Rate the background quality.
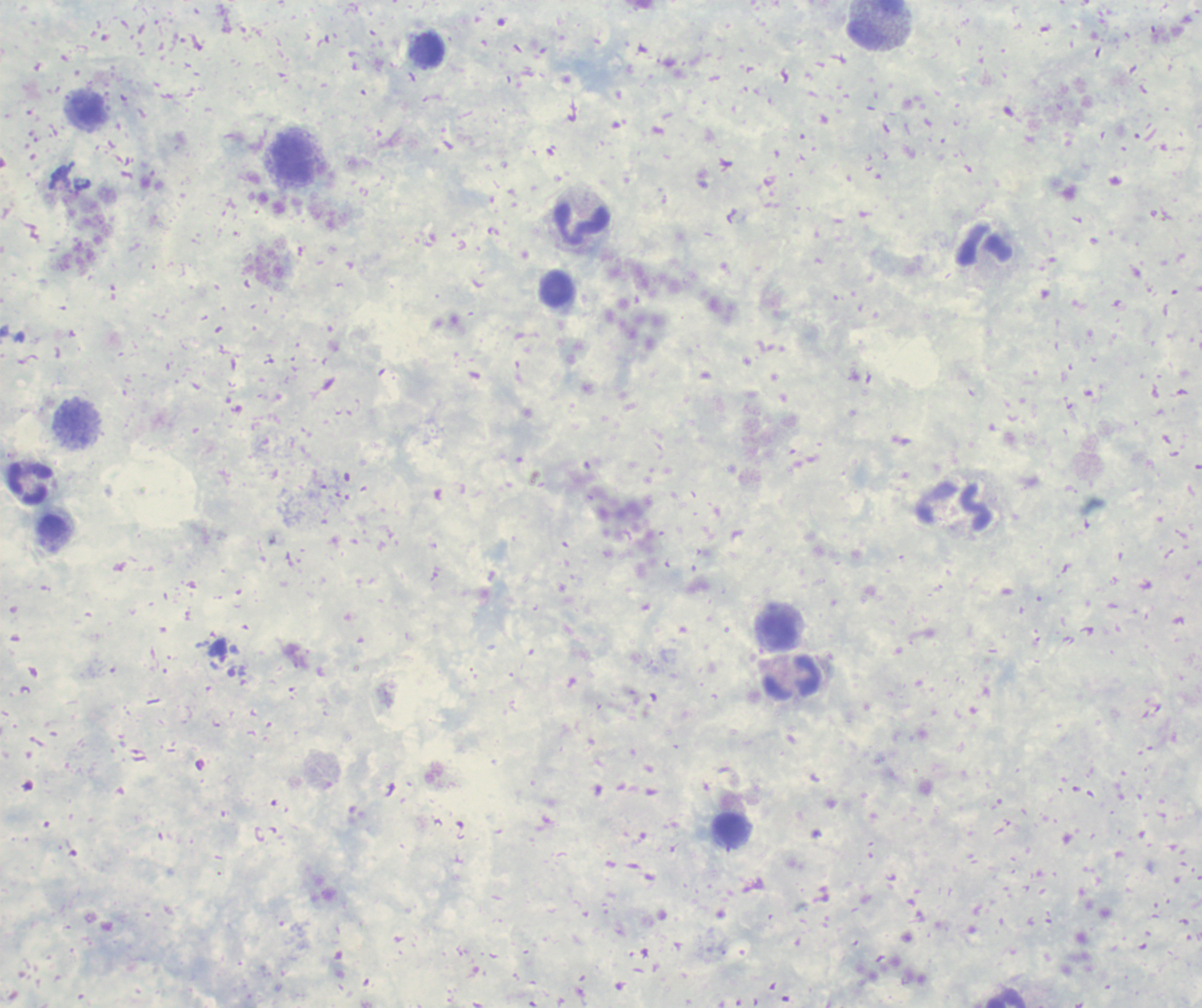

Unsatisfactory.

Approximate centers as {x, y} in pixels. Leukocyte locations: {877, 25}, {427, 52}, {293, 161}, {582, 225}, {984, 244}, {556, 289}, {77, 425}, {31, 484}, {954, 506}, {777, 631}, {793, 677}, {731, 831}. Romanowsky stain. Single field of view. Previously used in an actual diagnosis. Image is 1202×1008 pixels. Result: no Plasmodium parasites detected. Thick blood smear. Captured at 100x magnification.